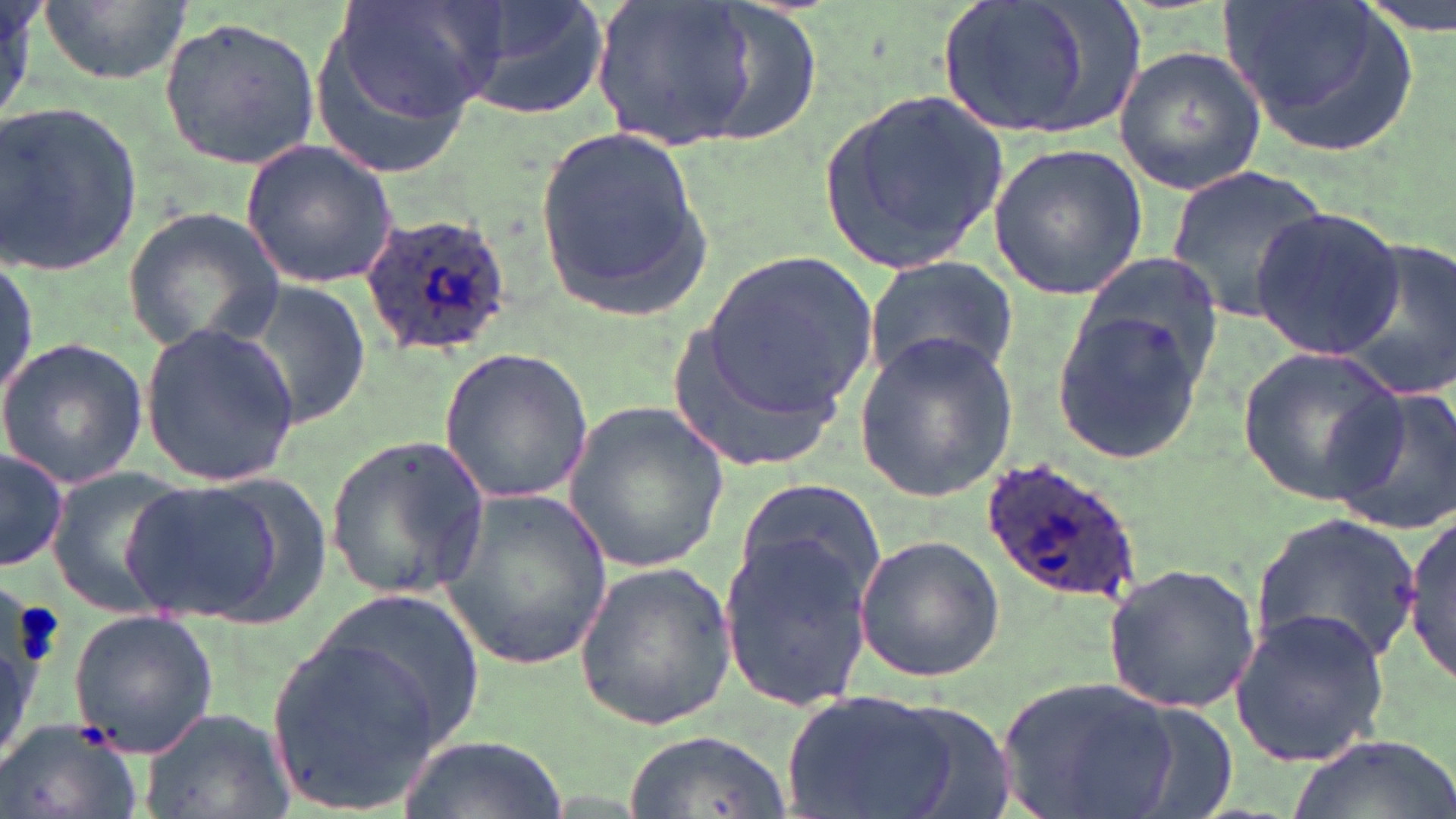 Approximate bounding boxes as (x1,y1)-(x2,y2) corner pairs in pixels. Platelet locations: (11,601)-(65,669). Plasmodium ovale-infected red blood cell locations: (360,210)-(514,361), (981,456)-(1145,604). Uninfected red blood cell locations: (36,0)-(195,87), (331,0)-(509,128), (451,0)-(612,119), (590,0)-(757,152), (929,0)-(1148,143), (1222,2)-(1421,158), (158,17)-(323,169), (306,27)-(480,181), (1112,44)-(1266,196), (816,89)-(1010,279), (2,102)-(147,275), (533,124)-(714,321), (241,139)-(400,290), (988,143)-(1148,300), (1166,168)-(1329,325), (123,204)-(284,350), (1251,209)-(1404,359), (1337,240)-(1456,402), (705,249)-(878,415), (1,254)-(38,408), (862,255)-(1021,387), (222,276)-(375,431), (1049,296)-(1210,466), (140,322)-(299,483), (664,322)-(849,471), (854,330)-(1019,499), (0,338)-(150,492), (1237,346)-(1407,505), (437,348)-(593,506), (1325,384)-(1456,536), (562,405)-(732,571), (326,433)-(490,599), (1,448)-(70,572), (51,474)-(202,619), (116,475)-(319,626), (731,482)-(888,618), (436,486)-(612,675), (1407,513)-(1456,684), (1250,515)-(1423,669), (718,522)-(879,709), (852,535)-(1004,682), (572,560)-(737,731), (1101,564)-(1261,713), (296,593)-(489,757), (1229,607)-(1392,769), (68,609)-(219,760), (265,638)-(447,811), (994,676)-(1188,817), (776,688)-(985,819), (139,705)-(294,819), (0,718)-(145,819), (627,728)-(789,816), (400,731)-(565,818), (1288,732)-(1456,819). Slide-level diagnosis: Plasmodium ovale. May-Grünwald-Giemsa-stained preparation. 1000x magnification. Thin blood smear. Image is 1456×819 pixels. One field of a larger specimen. Light microscopy.